Assess the morphology of the erythrocytes.
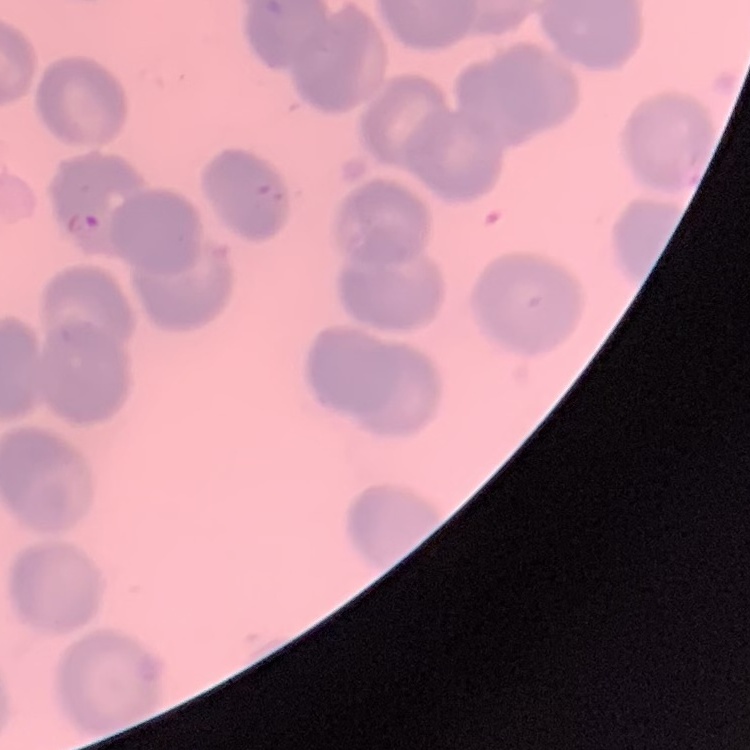
They show no rouleaux formation.

image type = one tile cut from a larger photomicrograph
stain = Field's or Giemsa
preparation = thin peripheral smear